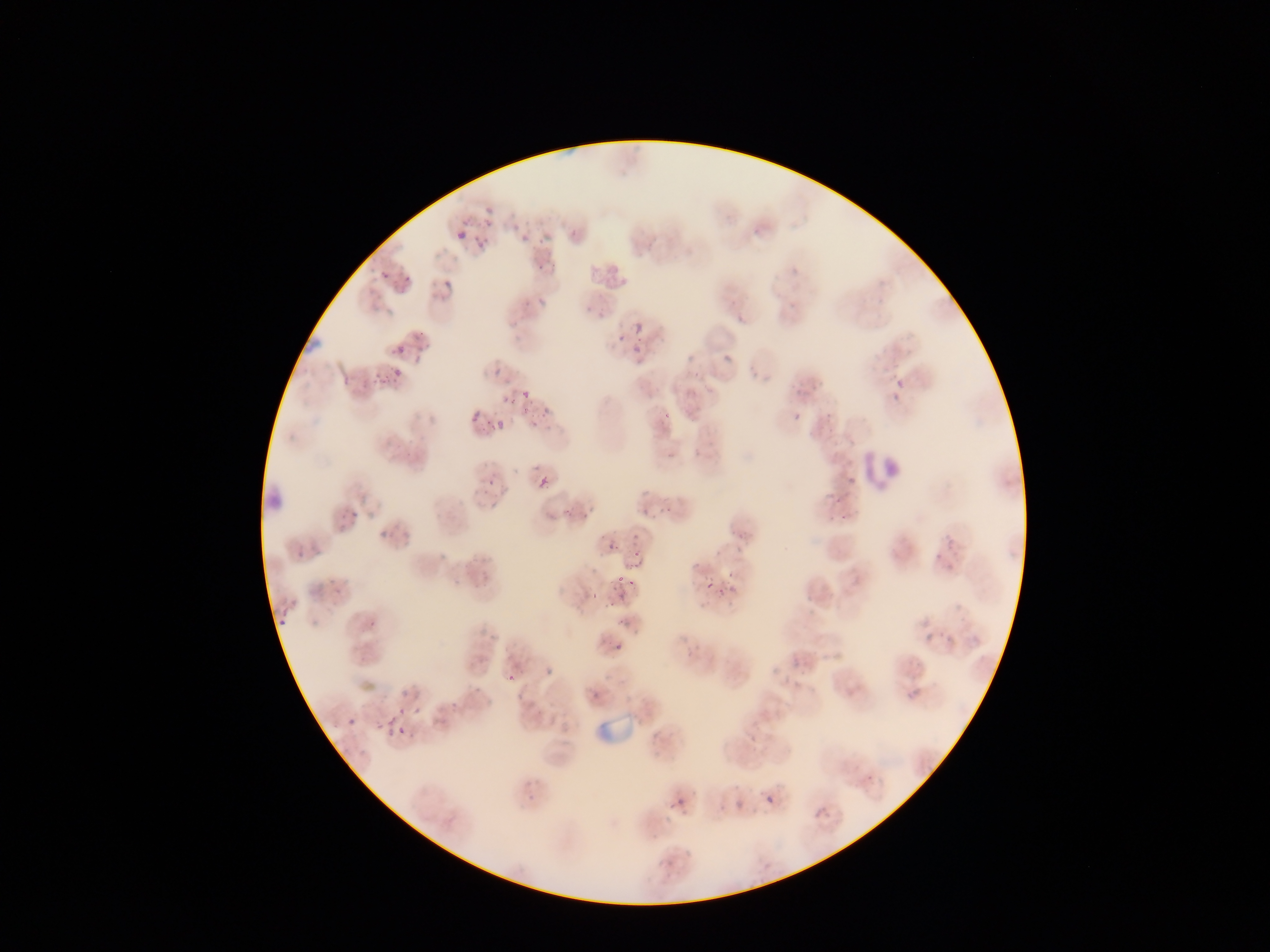
Approximate bounding boxes as [left, top, right, bottom] in pixels.
Summary:
  - Leukocyte locations: [855, 451, 911, 491]
  - Malaria parasite locations (subset; some below the resolvable size): [448, 205, 498, 250], [516, 230, 538, 244], [536, 259, 555, 276], [376, 268, 389, 283], [400, 276, 412, 290], [439, 282, 454, 297], [534, 299, 547, 312], [592, 300, 616, 320], [633, 322, 644, 334], [409, 326, 426, 345], [615, 333, 626, 344], [630, 342, 644, 356], [392, 343, 407, 357], [720, 346, 734, 372], [417, 355, 430, 365], [485, 359, 508, 377], [391, 367, 404, 381], [365, 370, 385, 387], [889, 371, 906, 406], [521, 388, 532, 401], [502, 396, 513, 406], [782, 406, 800, 420], [658, 408, 676, 422], [471, 412, 483, 419], [524, 412, 546, 429], [478, 472, 503, 493], [537, 476, 551, 491], [563, 500, 588, 518], [639, 501, 660, 522], [338, 508, 360, 529], [540, 514, 553, 525], [727, 518, 756, 542], [379, 521, 400, 538], [604, 540, 619, 556], [631, 542, 648, 554], [294, 543, 316, 563], [319, 566, 351, 594], [616, 566, 634, 600], [723, 568, 741, 593], [575, 578, 601, 606], [702, 579, 716, 593], [368, 607, 392, 628], [278, 610, 295, 631], [604, 643, 629, 663], [542, 664, 563, 683], [506, 670, 519, 685], [384, 686, 434, 739], [347, 718, 360, 732], [759, 782, 784, 813], [668, 794, 692, 817], [812, 801, 834, 818]
  - Field of view: single
  - Country: Ghana
  - Capture: mobile-phone photograph through a microscope
  - Preparation: thin blood film
  - Image size: 1270×952 pixels